Give the extent of all Plasmodium falciparum-infected red blood cells.
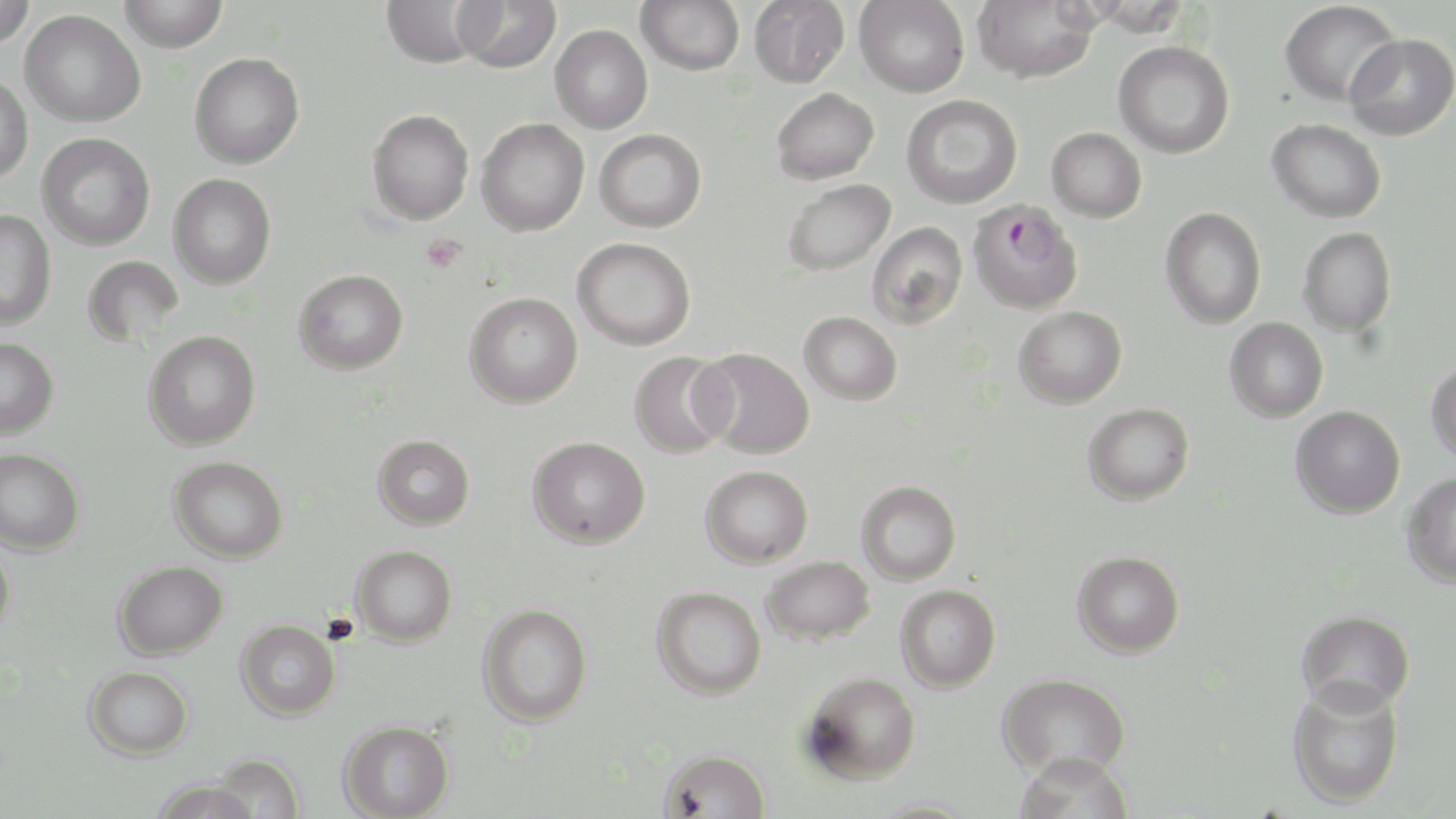

Approximate bounding boxes as (x1, y1, x2, y2) in pixels.
Plasmodium falciparum-infected red blood cells: (967, 199, 1084, 314).

slide-level diagnosis = Plasmodium falciparum
field of view = one of a larger specimen
platelet locations = approximate bounding boxes as (x1, y1, x2, y2) in pixels: (421, 233, 466, 274)
modality = light microscopy
image size = 1456×819 pixels
magnification = 1000x
stain = May-Grünwald-Giemsa
preparation = thin blood film
uninfected red blood cell locations = approximate bounding boxes as (x1, y1, x2, y2) in pixels: (0, 0, 38, 49), (118, 0, 228, 53), (380, 0, 486, 68), (454, 0, 562, 73), (636, 0, 745, 75), (748, 0, 850, 88), (854, 0, 969, 97), (972, 1, 1099, 82), (1279, 1, 1402, 107), (20, 9, 146, 127), (550, 24, 653, 133), (1344, 33, 1456, 140), (1113, 40, 1235, 158), (189, 52, 304, 169), (0, 73, 34, 186), (771, 87, 879, 184), (901, 94, 1022, 208), (367, 109, 474, 224), (476, 117, 589, 236), (1267, 118, 1386, 223), (1047, 127, 1147, 222), (594, 128, 707, 232), (37, 132, 155, 250), (168, 173, 277, 289), (781, 178, 895, 276), (1160, 206, 1266, 329), (0, 209, 57, 330), (867, 221, 968, 329), (1298, 227, 1396, 337), (572, 237, 696, 350), (82, 255, 185, 347), (294, 268, 409, 374), (464, 292, 583, 408), (1013, 305, 1127, 409), (799, 311, 903, 405), (1224, 317, 1328, 423), (143, 329, 262, 450), (0, 337, 59, 439), (693, 347, 815, 458), (628, 351, 735, 458), (1426, 361, 1456, 464), (1082, 402, 1195, 505), (1290, 405, 1405, 519), (372, 434, 475, 530), (527, 435, 651, 549), (0, 448, 85, 555), (169, 455, 288, 563), (699, 465, 813, 568), (1401, 471, 1456, 588), (856, 479, 962, 584), (0, 539, 15, 645), (352, 544, 458, 646), (1072, 550, 1184, 658), (761, 555, 875, 645), (113, 560, 228, 660), (895, 584, 1001, 692), (651, 585, 766, 699), (477, 603, 593, 727), (1296, 609, 1415, 714), (236, 619, 340, 721), (84, 665, 194, 760), (801, 670, 921, 784), (997, 672, 1131, 779), (1287, 679, 1405, 809), (339, 719, 455, 819), (659, 747, 771, 818), (210, 752, 306, 819), (1015, 752, 1137, 819), (149, 778, 261, 819), (865, 799, 983, 817)